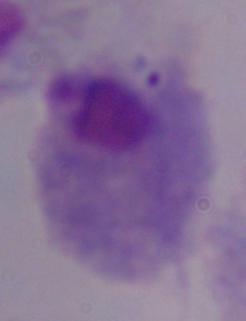

identification: trichomonad
magnification: 1000x
modality: micrograph